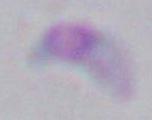

Toxoplasma gondii is seen. 1000x magnification. Photomicrograph.